Locate and identify every blood parasite.
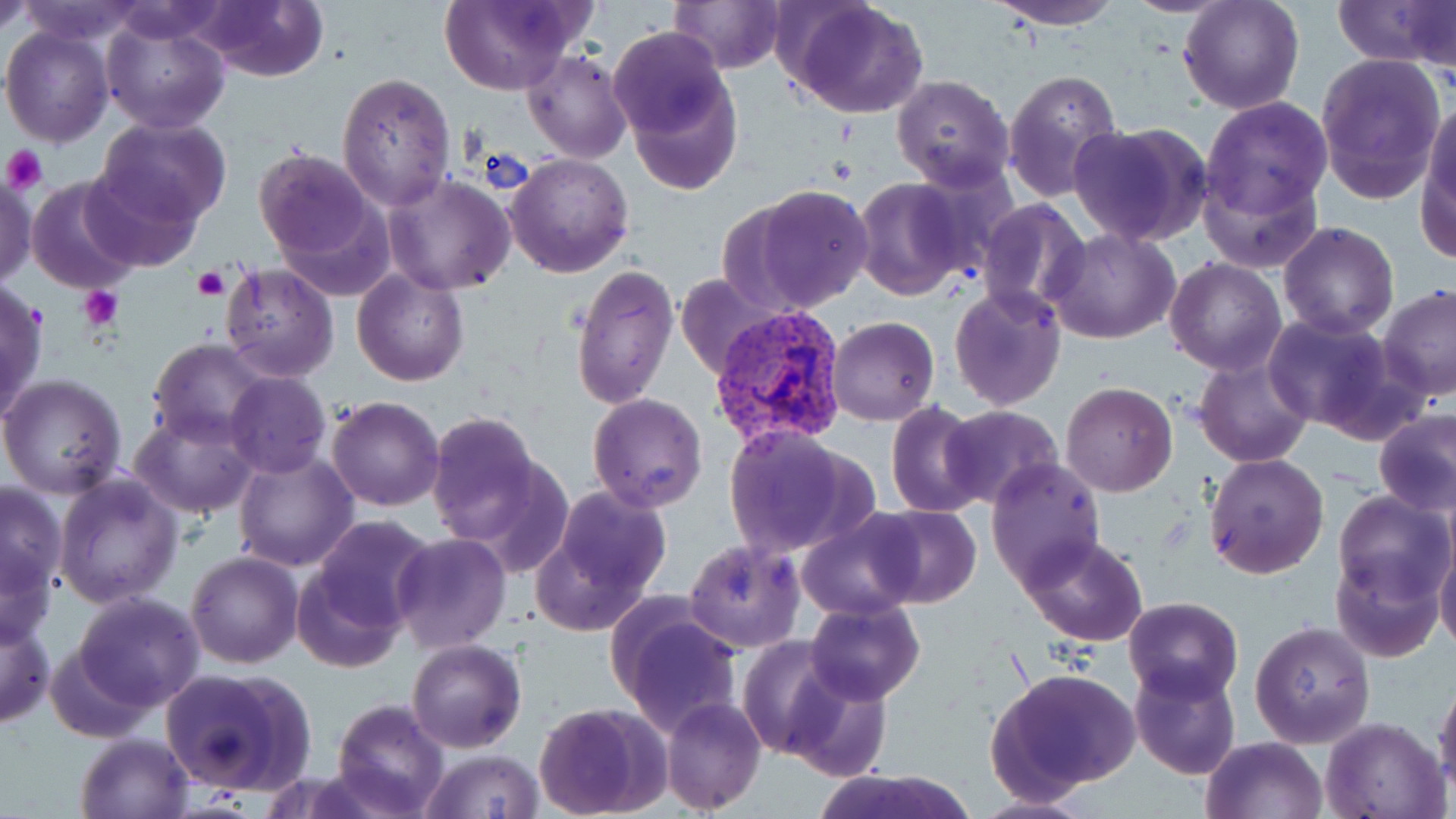
Approximate bounding boxes as named x1/y1/x2/y2 corners in pixels.
Plasmodium vivax-infected red blood cells: (x1=706, y1=305, x2=851, y2=452).
No Plasmodium falciparum, Plasmodium ovale, Plasmodium malariae, Babesia divergens, or Trypanosoma brucei observed.

Platelet locations: (x1=1, y1=144, x2=47, y2=194), (x1=193, y1=267, x2=230, y2=302), (x1=79, y1=286, x2=124, y2=331). Uninfected red blood cell locations: (x1=1, y1=0, x2=34, y2=35), (x1=15, y1=0, x2=145, y2=45), (x1=198, y1=0, x2=331, y2=83), (x1=440, y1=0, x2=583, y2=94), (x1=667, y1=0, x2=784, y2=73), (x1=786, y1=0, x2=929, y2=119), (x1=980, y1=0, x2=1130, y2=28), (x1=1119, y1=0, x2=1239, y2=16), (x1=1332, y1=0, x2=1456, y2=68), (x1=1179, y1=1, x2=1304, y2=115), (x1=1411, y1=1, x2=1455, y2=96), (x1=101, y1=15, x2=230, y2=134), (x1=2, y1=26, x2=114, y2=147), (x1=609, y1=28, x2=730, y2=142), (x1=523, y1=48, x2=631, y2=164), (x1=1315, y1=53, x2=1447, y2=204), (x1=1004, y1=68, x2=1123, y2=203), (x1=622, y1=71, x2=741, y2=198), (x1=336, y1=72, x2=456, y2=211), (x1=891, y1=74, x2=1015, y2=190), (x1=1201, y1=98, x2=1333, y2=218), (x1=1422, y1=98, x2=1456, y2=231), (x1=97, y1=116, x2=232, y2=232), (x1=1068, y1=122, x2=1211, y2=248), (x1=252, y1=146, x2=383, y2=267), (x1=505, y1=152, x2=634, y2=278), (x1=78, y1=162, x2=207, y2=275), (x1=1200, y1=162, x2=1323, y2=276), (x1=0, y1=172, x2=37, y2=289), (x1=383, y1=173, x2=515, y2=295), (x1=26, y1=174, x2=146, y2=296), (x1=852, y1=178, x2=971, y2=300), (x1=754, y1=185, x2=875, y2=311), (x1=977, y1=198, x2=1091, y2=317), (x1=1278, y1=220, x2=1399, y2=338), (x1=1047, y1=226, x2=1182, y2=345), (x1=1164, y1=256, x2=1287, y2=375), (x1=220, y1=264, x2=339, y2=383), (x1=569, y1=265, x2=679, y2=410), (x1=352, y1=269, x2=469, y2=386), (x1=679, y1=272, x2=777, y2=380), (x1=0, y1=279, x2=48, y2=423), (x1=950, y1=284, x2=1064, y2=409), (x1=1375, y1=284, x2=1456, y2=401), (x1=1263, y1=312, x2=1403, y2=435), (x1=826, y1=316, x2=940, y2=425), (x1=149, y1=339, x2=273, y2=448), (x1=1194, y1=353, x2=1314, y2=467), (x1=224, y1=372, x2=330, y2=477), (x1=0, y1=373, x2=127, y2=498), (x1=1060, y1=383, x2=1178, y2=497), (x1=588, y1=393, x2=709, y2=513), (x1=326, y1=396, x2=446, y2=511), (x1=886, y1=402, x2=987, y2=519), (x1=941, y1=406, x2=1064, y2=511), (x1=1374, y1=408, x2=1456, y2=515), (x1=130, y1=410, x2=257, y2=517), (x1=426, y1=413, x2=548, y2=547), (x1=724, y1=425, x2=857, y2=557), (x1=233, y1=449, x2=359, y2=572), (x1=1205, y1=452, x2=1329, y2=579), (x1=987, y1=456, x2=1107, y2=588), (x1=54, y1=472, x2=184, y2=610), (x1=1, y1=481, x2=67, y2=596), (x1=545, y1=485, x2=674, y2=612), (x1=1331, y1=490, x2=1453, y2=607), (x1=865, y1=504, x2=981, y2=609), (x1=798, y1=513, x2=924, y2=623), (x1=310, y1=515, x2=437, y2=635), (x1=389, y1=533, x2=511, y2=655), (x1=1435, y1=533, x2=1456, y2=655), (x1=1018, y1=534, x2=1149, y2=645), (x1=684, y1=538, x2=806, y2=653), (x1=0, y1=548, x2=57, y2=649), (x1=186, y1=551, x2=304, y2=669), (x1=1332, y1=551, x2=1443, y2=663), (x1=293, y1=561, x2=408, y2=674), (x1=72, y1=592, x2=204, y2=711), (x1=1123, y1=597, x2=1244, y2=703), (x1=610, y1=600, x2=744, y2=738), (x1=805, y1=601, x2=925, y2=705), (x1=0, y1=616, x2=54, y2=730), (x1=1250, y1=621, x2=1376, y2=748), (x1=735, y1=635, x2=849, y2=759), (x1=407, y1=638, x2=525, y2=752), (x1=47, y1=644, x2=152, y2=742), (x1=1129, y1=664, x2=1242, y2=780), (x1=157, y1=666, x2=314, y2=795), (x1=987, y1=667, x2=1140, y2=797), (x1=782, y1=670, x2=892, y2=781), (x1=1435, y1=672, x2=1456, y2=792), (x1=662, y1=696, x2=765, y2=815), (x1=333, y1=698, x2=450, y2=817), (x1=532, y1=702, x2=666, y2=817), (x1=1321, y1=717, x2=1449, y2=819), (x1=75, y1=732, x2=194, y2=819), (x1=1199, y1=736, x2=1328, y2=819), (x1=419, y1=749, x2=546, y2=819), (x1=811, y1=768, x2=976, y2=819), (x1=969, y1=794, x2=1097, y2=818). Slide-level diagnosis: Plasmodium vivax. Thin blood film. May-Grünwald-Giemsa-stained preparation. 1000x magnification. Light microscopy. Image is 1456×819 pixels. Single field of view.